Point out each Plasmodium parasite.
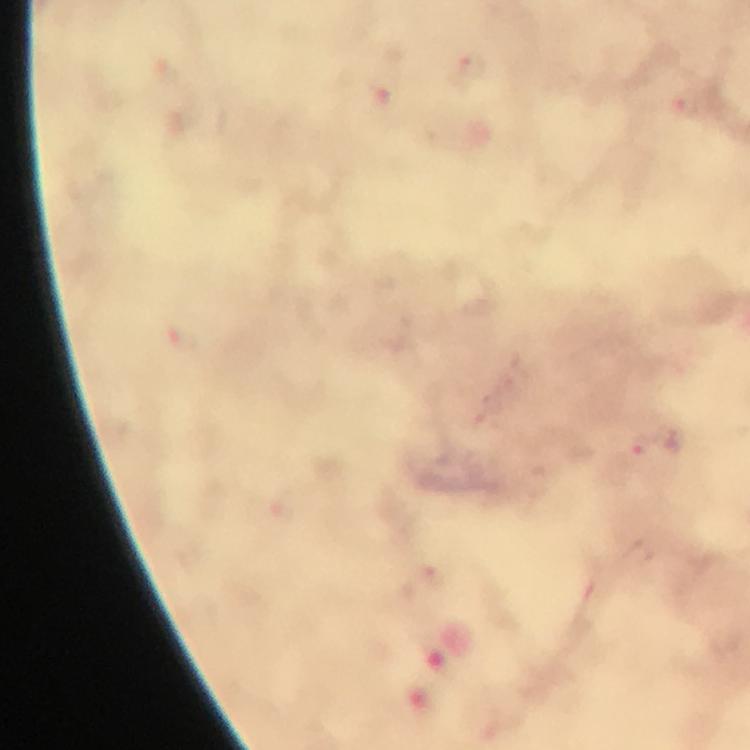

Approximate object centers, in pixels from the top-left corner.
Plasmodium parasites: (x=468, y=65), (x=688, y=103), (x=644, y=448).

Summary:
  - Preparation: thick blood smear
  - Image size: 750×750 pixels
  - Capture: smartphone camera through the microscope
  - Immersion oil: used
  - Cropped from: a single field of view
  - Magnification: 100x
  - Stain: Giemsa
  - Context: from a diagnostic examination for malaria